Assess the morphology of the erythrocytes.
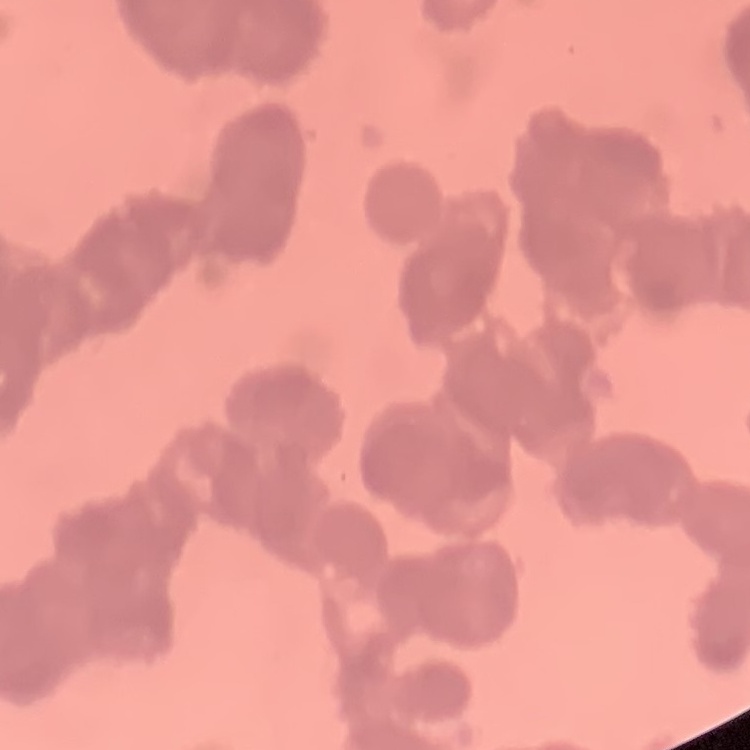

They show rouleaux formation.

{
  "stain": "Field's or Giemsa",
  "image_type": "one tile cut from a larger photomicrograph",
  "preparation": "thin blood smear"
}